Describe the morphology of the red blood cells.
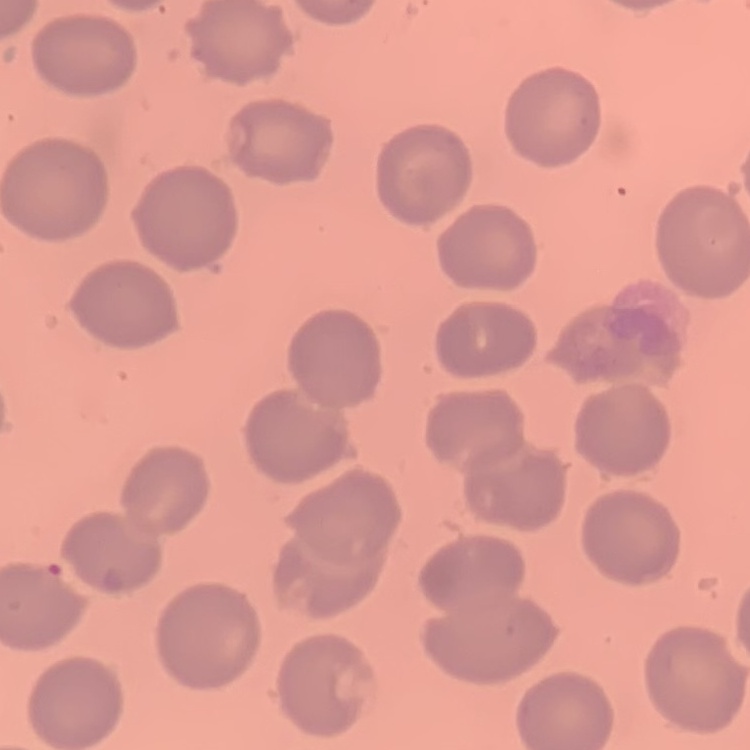
They show no rouleaux formation.

Thin blood film. Square crop of a larger photomicrograph. Stained with either Field's or Giemsa.